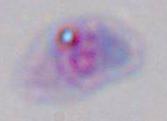

Summary:
  - Modality: micrograph
  - Magnification: 1000x
  - Identification: Toxoplasma gondii